Assess this cell for malaria.
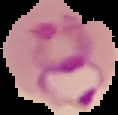

Parasitized.

Summary:
  - Preparation: thin blood film
  - Image size: 118×115 pixels
  - Image type: segmented cell region on a black background